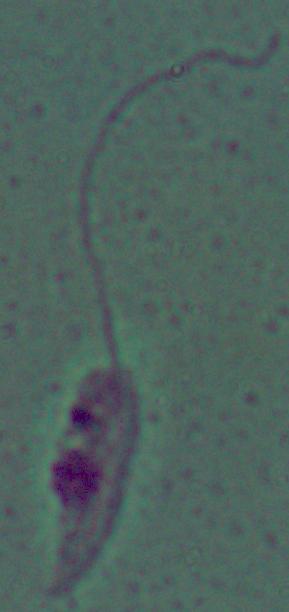
magnification = 1000x
identification = Leishmania
modality = micrograph